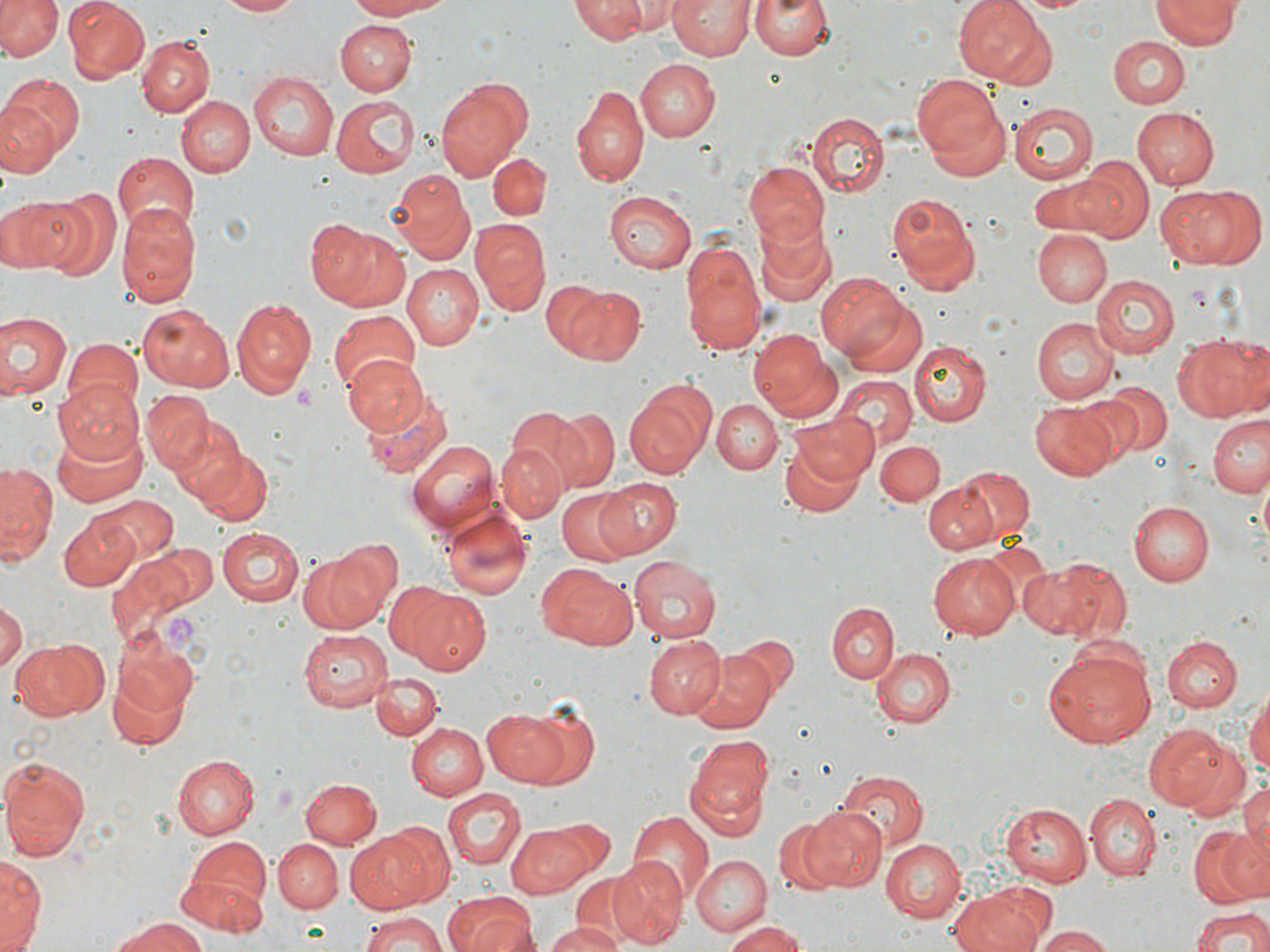
Summary:
  - Coordinate format: approximate bounding boxes as [x1, y1, x2, y2] in pixels
  - Plasmodium vivax-infected red blood cell locations: [358, 394, 451, 478]
  - Uninfected red blood cell locations: [0, 0, 64, 60], [62, 0, 147, 84], [216, 0, 307, 18], [342, 0, 450, 20], [570, 0, 649, 43], [596, 0, 680, 34], [748, 0, 835, 61], [956, 0, 1055, 86], [669, 1, 754, 60], [1154, 1, 1241, 48], [334, 19, 414, 95], [137, 35, 214, 116], [1107, 36, 1191, 107], [634, 58, 718, 142], [247, 72, 336, 159], [0, 74, 82, 167], [913, 76, 1010, 181], [436, 79, 529, 177], [574, 84, 648, 187], [176, 94, 255, 178], [332, 96, 416, 176], [1007, 103, 1098, 182], [1130, 106, 1218, 189], [807, 113, 890, 197], [110, 153, 197, 237], [485, 154, 551, 219], [1076, 156, 1154, 238], [744, 162, 829, 248], [391, 170, 475, 264], [1028, 172, 1120, 239], [1162, 183, 1260, 269], [33, 186, 119, 280], [603, 190, 695, 274], [885, 191, 980, 293], [1, 194, 75, 273], [117, 205, 203, 309], [752, 213, 836, 308], [302, 218, 409, 313], [471, 220, 550, 314], [1032, 229, 1111, 306], [679, 240, 768, 358], [401, 264, 483, 350], [815, 270, 913, 369], [1090, 272, 1179, 356], [541, 281, 610, 354], [557, 283, 644, 365], [230, 297, 317, 397], [843, 299, 928, 379], [135, 304, 236, 392], [327, 307, 421, 397], [0, 311, 69, 403], [1030, 318, 1119, 403], [748, 328, 838, 421], [1175, 334, 1269, 421], [61, 339, 144, 418], [911, 341, 990, 425], [343, 356, 429, 436], [835, 374, 917, 451], [53, 378, 144, 465], [1088, 380, 1173, 464], [624, 381, 715, 480], [141, 388, 214, 475], [714, 398, 783, 474], [1030, 400, 1123, 481], [504, 405, 592, 489], [545, 410, 617, 488], [787, 411, 878, 485], [1209, 412, 1270, 497], [51, 419, 150, 507], [173, 423, 254, 508], [777, 436, 866, 521], [875, 439, 945, 505], [406, 440, 500, 533], [496, 442, 566, 523], [189, 444, 273, 525], [1, 460, 58, 567], [952, 468, 1034, 543], [592, 476, 684, 557], [922, 481, 1000, 555], [557, 490, 635, 564], [90, 495, 178, 568], [1128, 501, 1214, 586], [440, 504, 532, 602], [60, 513, 137, 592], [216, 527, 305, 607], [331, 538, 404, 621], [109, 541, 216, 652], [297, 547, 390, 634], [928, 551, 1019, 639], [1019, 555, 1131, 644], [629, 556, 722, 643], [536, 563, 637, 650], [394, 583, 489, 673], [0, 600, 24, 678], [827, 602, 899, 684], [297, 628, 393, 710], [1162, 635, 1240, 712], [647, 636, 726, 717], [9, 638, 106, 721], [871, 647, 956, 729], [1042, 648, 1157, 748], [691, 649, 776, 733], [108, 651, 194, 752], [372, 671, 442, 740], [1245, 691, 1270, 781], [486, 706, 594, 791], [406, 722, 487, 798], [1143, 723, 1233, 813], [686, 735, 773, 835], [171, 754, 260, 838], [0, 756, 91, 862], [834, 768, 929, 852], [1239, 777, 1270, 852], [299, 778, 381, 849], [442, 789, 525, 870], [1085, 794, 1159, 880], [1004, 801, 1096, 885], [800, 804, 887, 891], [629, 810, 714, 900], [774, 817, 846, 895], [507, 821, 602, 897], [1191, 824, 1270, 908], [343, 829, 439, 914], [179, 838, 272, 928], [883, 838, 968, 921], [274, 839, 343, 913], [692, 854, 773, 936], [1, 855, 44, 951], [607, 855, 688, 947], [570, 876, 642, 946], [954, 885, 1058, 952], [443, 890, 537, 952], [1188, 906, 1270, 952], [359, 910, 450, 952], [110, 918, 208, 952], [722, 919, 810, 952], [545, 923, 624, 952], [1032, 927, 1116, 952]
  - Platelet locations: [293, 381, 317, 412], [162, 614, 198, 648]
  - Slide-level diagnosis: Plasmodium vivax
  - Field of view: one of a larger specimen
  - Stain: May-Grünwald-Giemsa
  - Image size: 1270×952 pixels
  - Preparation: thin blood smear
  - Modality: light microscopy
  - Magnification: 1000x